Identify the parasite.
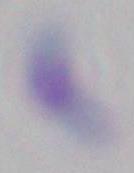

This is Toxoplasma gondii.

Summary:
  - Magnification: 1000x
  - Modality: micrograph